Name the parasite shown.
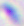

Toxoplasma gondii.

magnification = 400x
modality = micrograph